State which parasite is depicted.
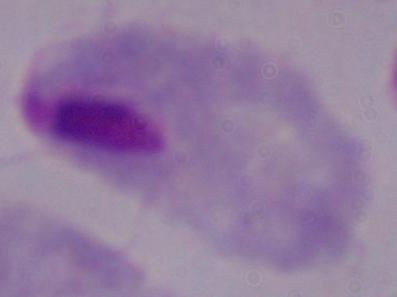
This is a trichomonad.

Micrograph. Captured at 1000x magnification.